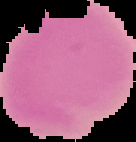
{
  "image_size": "136×142 pixels",
  "image_type": "segmented cell region with the area outside set to black",
  "malaria_status": "uninfected",
  "preparation": "thin blood film"
}